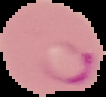

Image is 106×97 pixels. From a thin blood film. Segmented cell region on a black background. Malaria status: parasitized.